Name the malaria species.
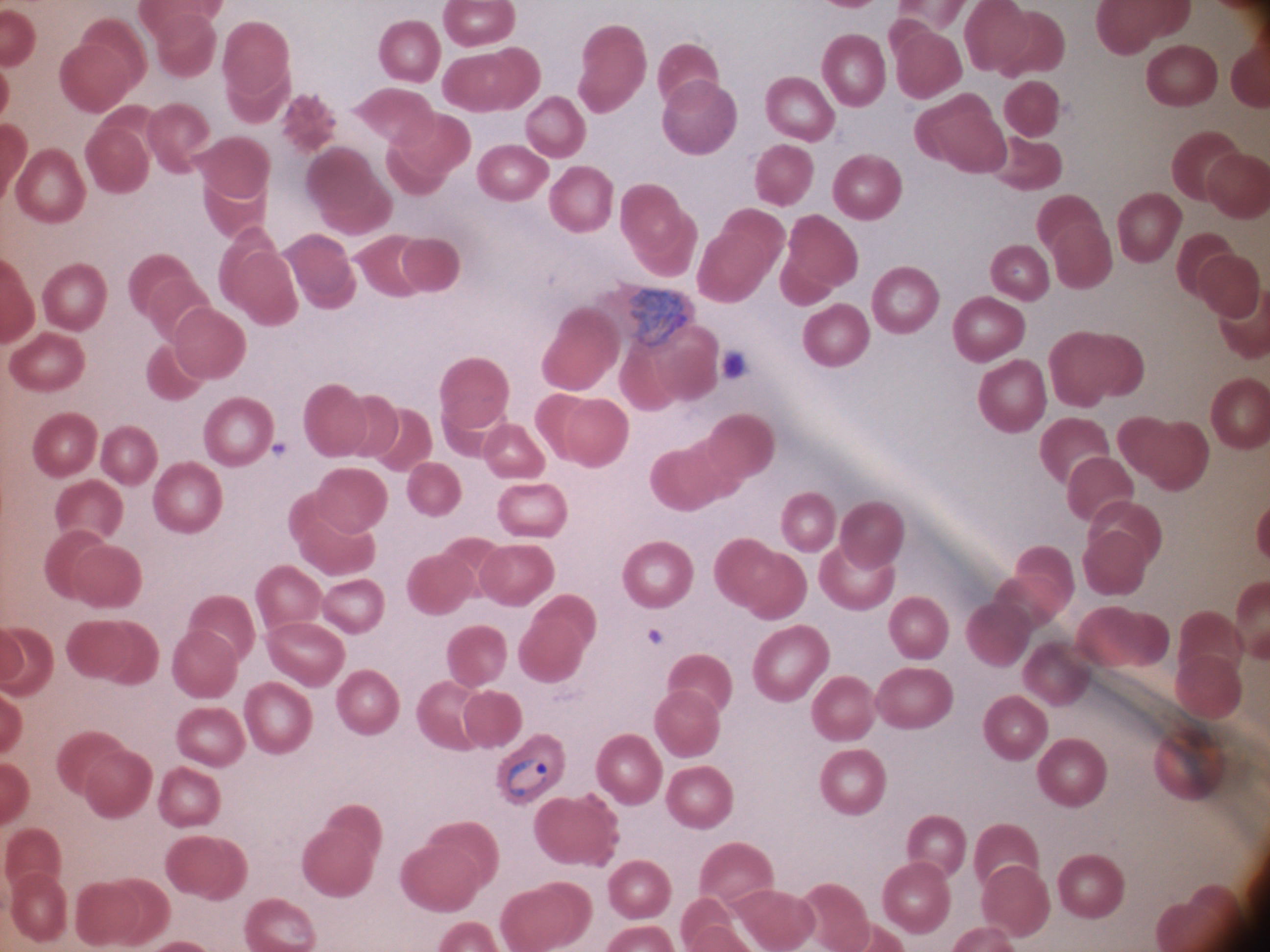

Plasmodium ovale.

Approximate bounding boxes as [x1, y1, x2, y2] in pixels, from the source annotation, which is not necessarily exhaustive. Malaria parasite locations: [627, 287, 691, 349], [506, 758, 548, 797]. Life-cycle stages among the annotated parasites: ring form, trophozoite. Single field of view. Leica DM2000 optical microscope with a built-in camera. Image is 1270×952 pixels. 100x magnification. Thin blood smear. Giemsa-stained preparation.